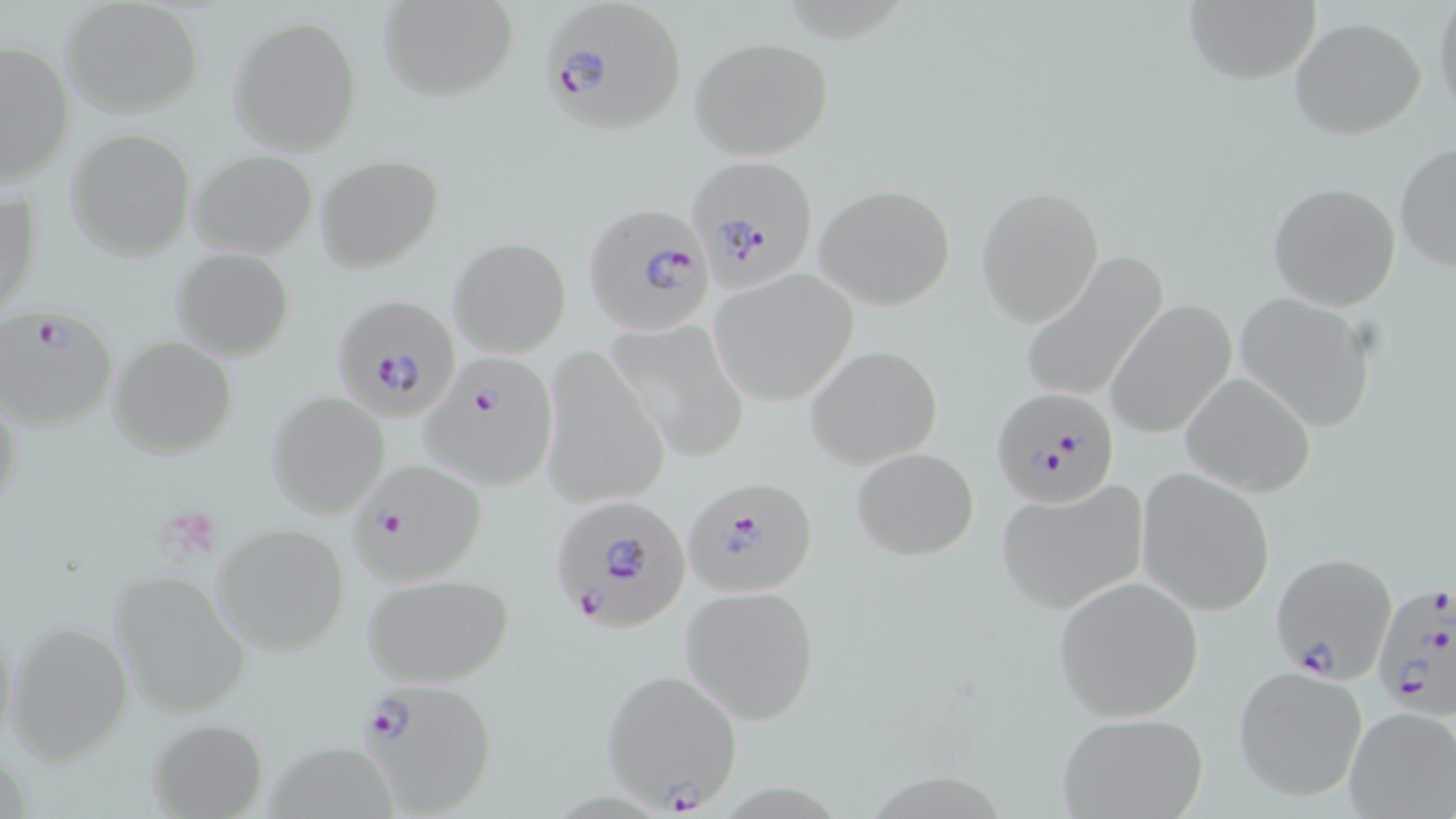

{
  "slide_level_diagnosis": "Plasmodium falciparum",
  "field_of_view": "one of a larger specimen",
  "preparation": "thin blood film",
  "stain": "May-Grünwald-Giemsa",
  "plasmodium_falciparum_infected_red_blood_cell_locations": "approximate bounding boxes as [x1, y1, x2, y2] in pixels: [538, 1, 690, 138], [689, 156, 819, 289], [585, 203, 716, 335], [330, 293, 462, 419], [0, 307, 117, 433], [427, 352, 555, 490], [990, 384, 1120, 508], [349, 461, 490, 585], [683, 476, 816, 597], [551, 496, 692, 634], [1272, 551, 1395, 683], [1373, 579, 1455, 719], [600, 667, 744, 811], [356, 678, 496, 814]",
  "platelet_locations": "approximate bounding boxes as [x1, y1, x2, y2] in pixels: [165, 509, 227, 567]",
  "uninfected_red_blood_cell_locations": "approximate bounding boxes as [x1, y1, x2, y2] in pixels: [61, 0, 203, 116], [377, 0, 519, 101], [1431, 0, 1455, 120], [1181, 1, 1321, 84], [228, 16, 362, 155], [1289, 16, 1426, 139], [689, 35, 834, 162], [1, 40, 75, 185], [67, 127, 195, 259], [1394, 142, 1455, 271], [187, 149, 319, 258], [315, 155, 444, 274], [1267, 180, 1402, 311], [814, 183, 955, 309], [976, 185, 1105, 328], [1, 186, 39, 321], [448, 236, 571, 357], [172, 247, 294, 361], [1021, 251, 1167, 404], [709, 270, 858, 407], [1233, 292, 1378, 433], [1106, 300, 1237, 439], [606, 314, 750, 464], [107, 336, 237, 457], [805, 344, 943, 468], [540, 348, 672, 511], [1180, 373, 1316, 495], [268, 391, 390, 518], [0, 392, 24, 527], [850, 447, 979, 561], [1136, 467, 1277, 616], [993, 481, 1148, 616], [213, 523, 349, 654], [106, 569, 251, 719], [362, 572, 516, 687], [1051, 575, 1206, 722], [682, 585, 820, 724], [4, 621, 134, 764], [1233, 667, 1365, 801], [1342, 706, 1455, 819], [1056, 711, 1208, 818], [148, 717, 266, 817]",
  "image_size": "1456×819 pixels",
  "magnification": "1000x",
  "modality": "optical microscopy"
}